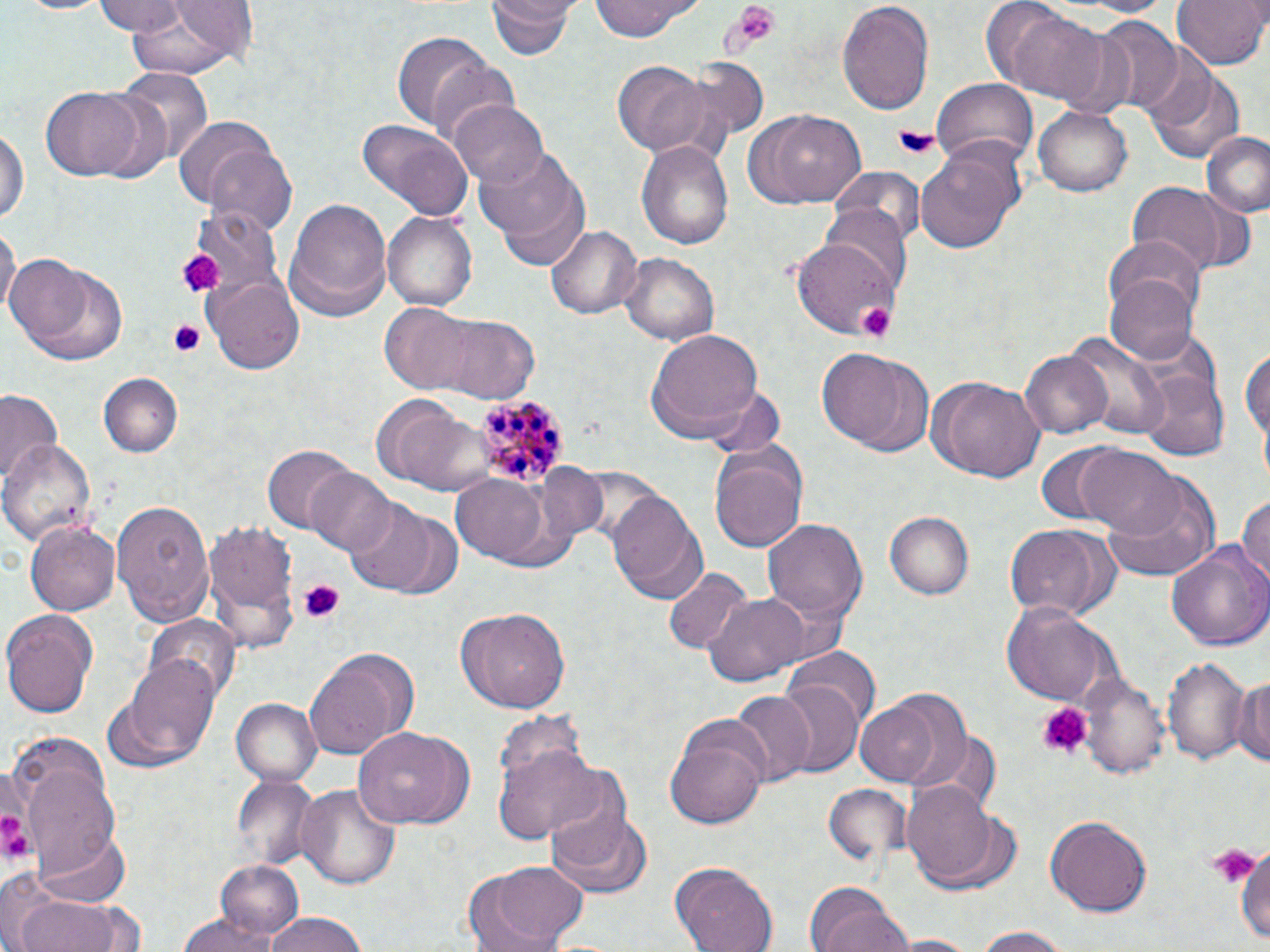 Approximate bounding boxes as named x1/y1/x2/y2 corners in pixels. Plasmodium malariae-infected red blood cell locations: (x1=472, y1=394, x2=570, y2=487). Uninfected red blood cell locations: (x1=8, y1=0, x2=113, y2=15), (x1=94, y1=0, x2=190, y2=35), (x1=487, y1=0, x2=575, y2=61), (x1=981, y1=0, x2=1084, y2=98), (x1=1171, y1=0, x2=1268, y2=71), (x1=588, y1=1, x2=706, y2=41), (x1=837, y1=2, x2=934, y2=120), (x1=118, y1=3, x2=252, y2=82), (x1=1091, y1=16, x2=1183, y2=116), (x1=1049, y1=22, x2=1138, y2=117), (x1=390, y1=29, x2=495, y2=130), (x1=420, y1=51, x2=524, y2=144), (x1=613, y1=61, x2=711, y2=155), (x1=117, y1=66, x2=214, y2=164), (x1=1152, y1=71, x2=1245, y2=166), (x1=930, y1=77, x2=1037, y2=171), (x1=40, y1=87, x2=148, y2=181), (x1=451, y1=100, x2=548, y2=189), (x1=743, y1=106, x2=866, y2=209), (x1=1033, y1=107, x2=1131, y2=196), (x1=174, y1=116, x2=286, y2=217), (x1=357, y1=119, x2=474, y2=220), (x1=1, y1=124, x2=28, y2=225), (x1=1203, y1=132, x2=1270, y2=216), (x1=640, y1=140, x2=734, y2=249), (x1=205, y1=144, x2=296, y2=236), (x1=477, y1=144, x2=591, y2=265), (x1=916, y1=149, x2=1019, y2=255), (x1=828, y1=167, x2=927, y2=246), (x1=1127, y1=183, x2=1230, y2=276), (x1=283, y1=197, x2=393, y2=321), (x1=820, y1=202, x2=911, y2=295), (x1=189, y1=204, x2=283, y2=297), (x1=384, y1=209, x2=479, y2=311), (x1=1, y1=221, x2=19, y2=322), (x1=546, y1=223, x2=642, y2=321), (x1=1104, y1=237, x2=1206, y2=328), (x1=792, y1=241, x2=904, y2=340), (x1=621, y1=253, x2=720, y2=346), (x1=6, y1=254, x2=126, y2=365), (x1=1105, y1=270, x2=1199, y2=365), (x1=205, y1=274, x2=306, y2=373), (x1=375, y1=307, x2=489, y2=396), (x1=420, y1=315, x2=541, y2=401), (x1=646, y1=326, x2=765, y2=439), (x1=1067, y1=331, x2=1171, y2=440), (x1=1239, y1=344, x2=1269, y2=466), (x1=819, y1=348, x2=934, y2=455), (x1=1021, y1=349, x2=1112, y2=438), (x1=1138, y1=368, x2=1228, y2=459), (x1=99, y1=374, x2=181, y2=457), (x1=928, y1=375, x2=1046, y2=484), (x1=698, y1=384, x2=786, y2=461), (x1=0, y1=392, x2=61, y2=488), (x1=369, y1=398, x2=498, y2=496), (x1=1, y1=439, x2=94, y2=548), (x1=707, y1=442, x2=809, y2=554), (x1=1033, y1=444, x2=1133, y2=528), (x1=263, y1=445, x2=357, y2=532), (x1=1072, y1=446, x2=1184, y2=536), (x1=537, y1=463, x2=607, y2=542), (x1=310, y1=466, x2=398, y2=557), (x1=452, y1=474, x2=550, y2=561), (x1=1100, y1=477, x2=1220, y2=585), (x1=608, y1=489, x2=706, y2=599), (x1=1236, y1=489, x2=1270, y2=592), (x1=110, y1=500, x2=214, y2=625), (x1=344, y1=500, x2=435, y2=592), (x1=883, y1=511, x2=973, y2=600), (x1=763, y1=517, x2=867, y2=628), (x1=25, y1=518, x2=119, y2=618), (x1=204, y1=518, x2=299, y2=651), (x1=1002, y1=524, x2=1120, y2=622), (x1=1166, y1=541, x2=1270, y2=654), (x1=664, y1=569, x2=752, y2=656), (x1=705, y1=590, x2=808, y2=686), (x1=1000, y1=601, x2=1121, y2=706), (x1=453, y1=605, x2=570, y2=714), (x1=2, y1=609, x2=98, y2=717), (x1=146, y1=615, x2=241, y2=708), (x1=784, y1=647, x2=881, y2=731), (x1=303, y1=649, x2=416, y2=759), (x1=1161, y1=651, x2=1253, y2=767), (x1=120, y1=656, x2=220, y2=766), (x1=1079, y1=672, x2=1171, y2=779), (x1=1234, y1=672, x2=1270, y2=773), (x1=773, y1=677, x2=865, y2=777), (x1=730, y1=691, x2=814, y2=786), (x1=232, y1=699, x2=321, y2=787), (x1=853, y1=699, x2=944, y2=787), (x1=665, y1=716, x2=770, y2=829), (x1=352, y1=727, x2=473, y2=830), (x1=492, y1=738, x2=603, y2=846), (x1=18, y1=759, x2=125, y2=882), (x1=545, y1=773, x2=636, y2=870), (x1=232, y1=775, x2=321, y2=872), (x1=294, y1=782, x2=401, y2=892), (x1=901, y1=782, x2=1002, y2=886), (x1=823, y1=783, x2=912, y2=881), (x1=546, y1=809, x2=655, y2=899), (x1=1046, y1=816, x2=1153, y2=915), (x1=37, y1=826, x2=133, y2=909), (x1=1234, y1=839, x2=1270, y2=951), (x1=215, y1=861, x2=305, y2=941), (x1=464, y1=861, x2=589, y2=951), (x1=670, y1=863, x2=778, y2=952), (x1=802, y1=885, x2=911, y2=952), (x1=9, y1=891, x2=137, y2=952), (x1=262, y1=912, x2=372, y2=952), (x1=179, y1=915, x2=274, y2=952), (x1=967, y1=925, x2=1078, y2=951), (x1=886, y1=934, x2=985, y2=951). Platelet locations: (x1=729, y1=3, x2=782, y2=52), (x1=893, y1=123, x2=942, y2=162), (x1=176, y1=250, x2=221, y2=298), (x1=858, y1=303, x2=897, y2=344), (x1=165, y1=320, x2=208, y2=359), (x1=297, y1=579, x2=346, y2=622), (x1=1035, y1=703, x2=1093, y2=762), (x1=0, y1=810, x2=28, y2=857), (x1=1205, y1=845, x2=1255, y2=891). Slide-level diagnosis: Plasmodium malariae. Thin blood smear. Image is 1270×952 pixels. May-Grünwald-Giemsa stain. Light microscopy. One field of a larger specimen. Captured at 1000x magnification.